Outline each uninfected red blood cell.
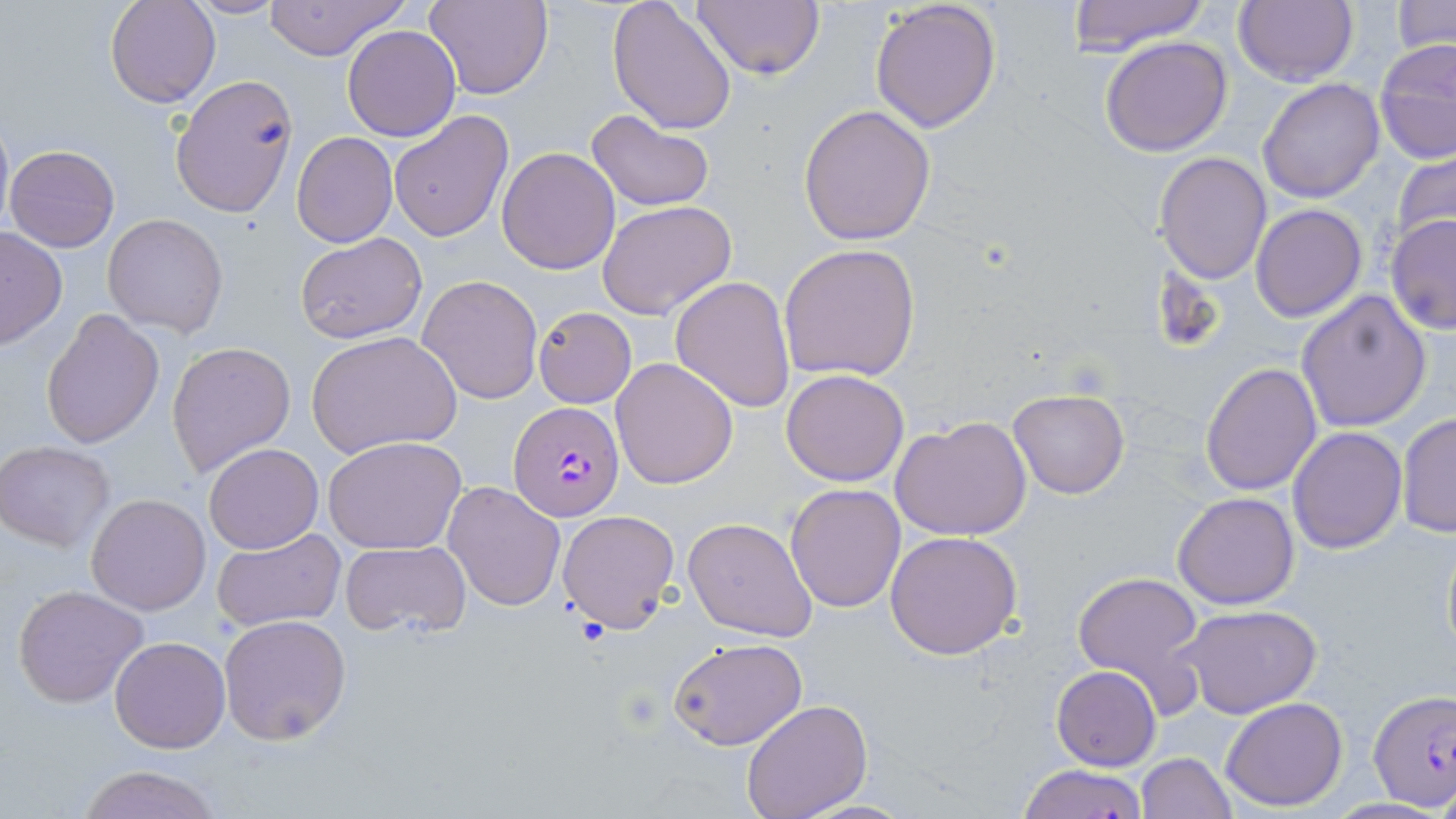
Approximate bounding boxes as (x1, y1, x2, y2) in pixels.
Uninfected red blood cells: (105, 0, 220, 108), (183, 0, 285, 18), (263, 0, 409, 60), (424, 0, 552, 100), (608, 0, 737, 135), (689, 0, 825, 82), (1065, 0, 1209, 55), (869, 1, 1003, 135), (1231, 1, 1360, 88), (1393, 1, 1454, 55), (342, 24, 460, 139), (1099, 36, 1232, 157), (1374, 40, 1456, 166), (169, 75, 300, 220), (1258, 79, 1386, 203), (797, 105, 937, 248), (586, 109, 715, 213), (387, 110, 512, 244), (291, 132, 397, 247), (5, 143, 120, 252), (496, 147, 621, 274), (1392, 148, 1456, 252), (1155, 151, 1272, 286), (596, 199, 738, 319), (1251, 203, 1367, 321), (103, 212, 230, 337), (1385, 215, 1456, 335), (0, 227, 67, 349), (295, 231, 428, 345), (777, 243, 921, 381), (417, 274, 543, 406), (670, 275, 797, 414), (1295, 290, 1433, 432), (533, 307, 637, 408), (40, 309, 165, 450), (306, 330, 462, 458), (166, 339, 296, 478), (610, 356, 740, 489), (1201, 362, 1322, 498), (780, 369, 909, 486), (1008, 389, 1130, 498), (1397, 412, 1455, 538), (890, 416, 1032, 542), (1287, 425, 1406, 553), (323, 436, 467, 554), (0, 441, 115, 551), (203, 443, 324, 553), (442, 479, 566, 613), (785, 484, 906, 612), (1171, 492, 1299, 610), (86, 493, 211, 615), (556, 510, 680, 632), (684, 517, 818, 642), (1440, 524, 1455, 671), (211, 527, 345, 632), (884, 531, 1025, 660), (339, 540, 472, 639), (1072, 569, 1206, 699), (13, 585, 149, 707), (1179, 604, 1322, 718), (218, 613, 351, 744), (110, 637, 230, 754), (667, 638, 807, 751), (1052, 665, 1161, 771), (1220, 697, 1348, 809), (740, 699, 872, 819), (1137, 752, 1237, 818), (75, 764, 223, 819), (1014, 764, 1151, 819), (788, 797, 922, 818), (1325, 798, 1450, 818).

Plasmodium falciparum-infected red blood cell locations: (511, 403, 623, 522), (1368, 692, 1455, 807). Slide-level diagnosis: Plasmodium falciparum. Optical microscopy. Image is 1456×819 pixels. Thin blood smear. Captured at 1000x magnification. May-Grünwald-Giemsa stain. Single field of view.